Report the malaria status of this cell.
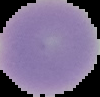
Uninfected.

Summary:
  - Preparation: thin blood film
  - Image size: 100×97 pixels
  - Image type: segmented cell region with the area outside set to black